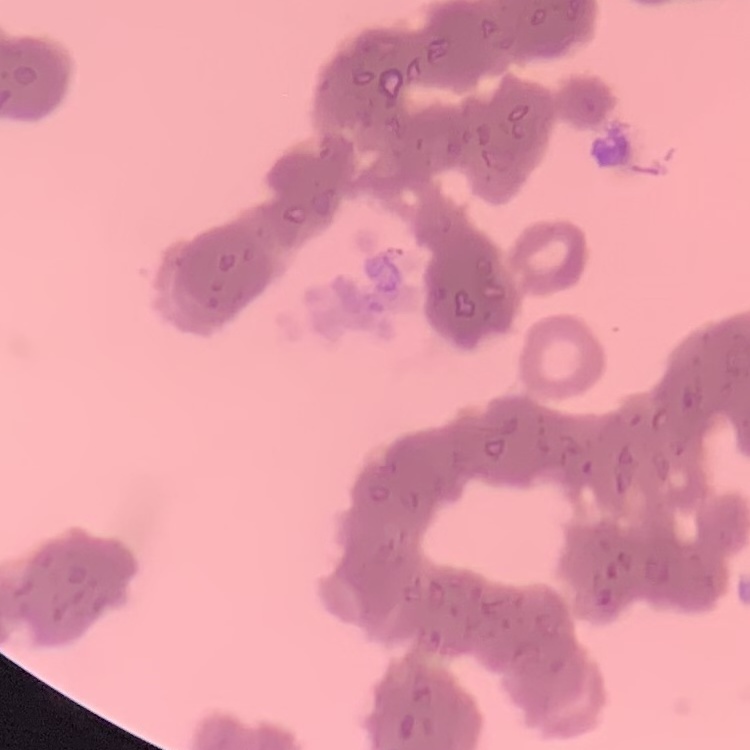
Summary:
  - Red blood cell morphology: rouleaux formation
  - Image type: square crop of a larger photomicrograph
  - Stain: Field's or Giemsa
  - Preparation: thin blood smear